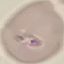
Summary:
  - Result: malaria parasites identified
  - Image type: automatically extracted cell patch, resized to 64 × 64 pixels
  - Preparation: thin blood film
  - Capture: smartphone camera at the microscope eyepiece
  - Stain: Giemsa